Assess this cell for malaria.
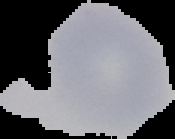
Uninfected.

image size = 175×139 pixels
preparation = thin blood film
image type = segmented cell region with the area outside set to black